Identify the cell.
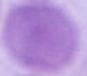

An erythrocyte.

modality = photomicrograph
magnification = 1000x